Classify this cell by malaria status.
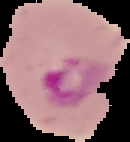

Parasitized.

Cell region segmented out of the field of view; the surrounding area is masked to black. Image is 130×142 pixels. From a thin blood smear.